State which parasite is depicted.
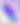
This is Toxoplasma gondii.

Summary:
  - Magnification: 400x
  - Modality: photomicrograph